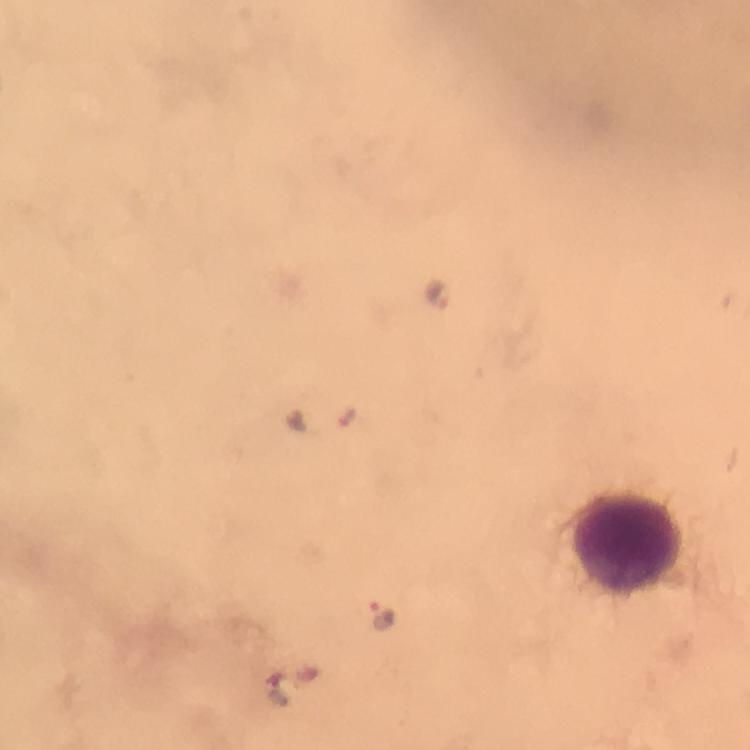

capture = smartphone photograph through a microscope
context = from a malaria diagnostic workup
magnification = 100x
malaria parasite locations = approximate centers as (x, y) in pixels: (438, 294), (381, 614), (280, 694)
immersion oil = applied
image size = 750×750 pixels
cropped from = one field of view
preparation = thick blood film
leukocyte locations = approximate centers as (x, y) in pixels: (630, 546)
stain = Giemsa